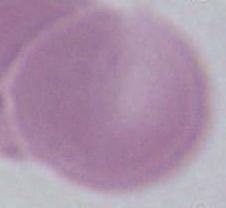
Summary:
  - Identification: red blood cell
  - Magnification: 1000x
  - Modality: micrograph